Locate and identify every blood parasite.
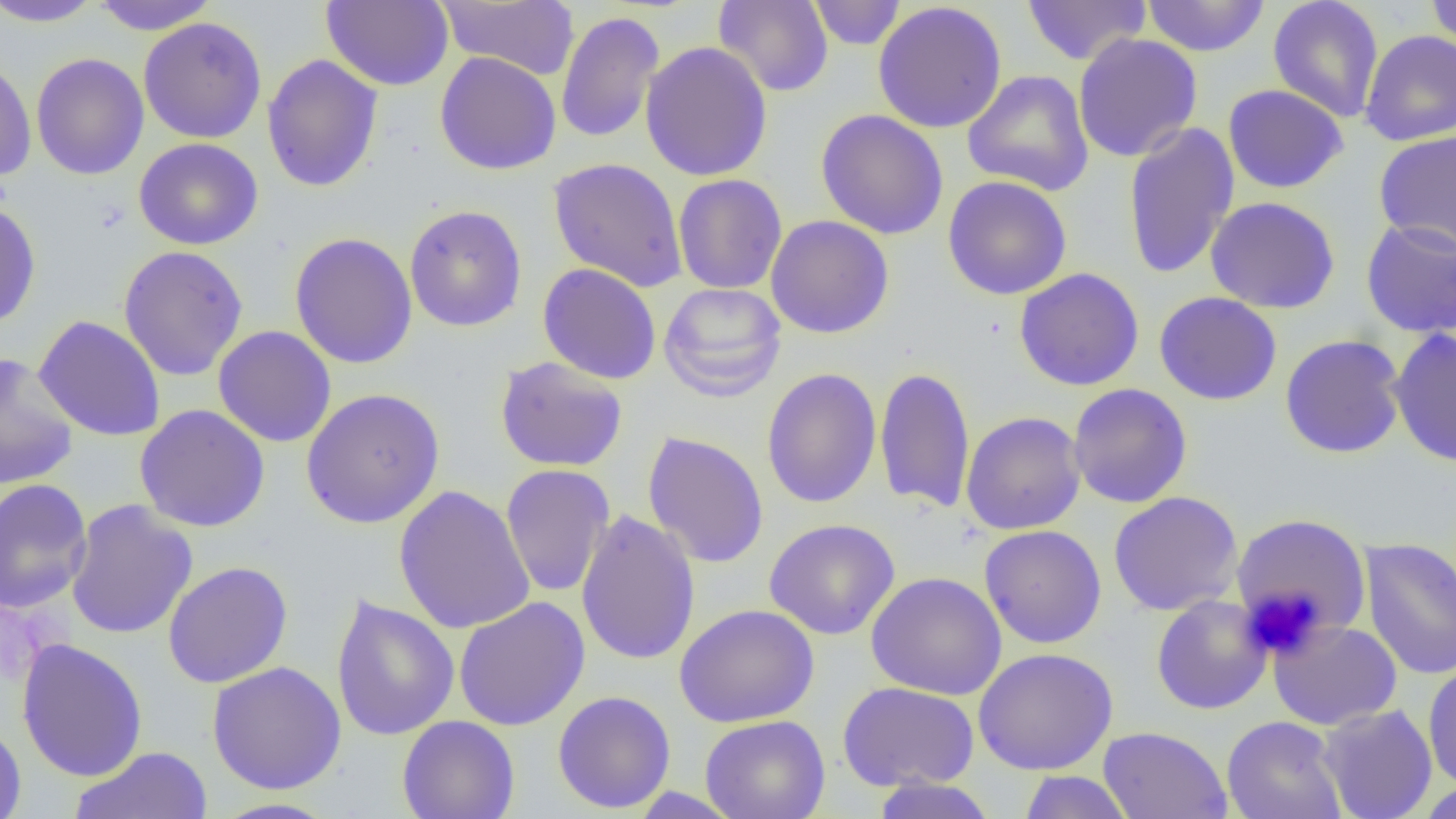

No blood parasites seen.

Approximate bounding boxes as (x1,y1)-(x2,y2) corner pairs in pixels. Platelet locations: (1242,587)-(1326,659). Uninfected red blood cell locations: (0,0)-(105,28), (89,0)-(220,35), (322,0)-(453,90), (437,0)-(579,80), (713,0)-(834,97), (807,0)-(906,50), (1021,0)-(1152,66), (1141,0)-(1270,57), (1425,0)-(1456,53), (1268,1)-(1384,123), (872,2)-(1008,134), (555,10)-(665,144), (138,17)-(267,144), (1360,29)-(1456,146), (1072,33)-(1203,162), (640,41)-(773,182), (434,52)-(562,175), (30,53)-(149,180), (0,54)-(37,182), (262,54)-(383,193), (962,70)-(1094,196), (1223,84)-(1349,193), (815,109)-(949,240), (1122,121)-(1239,281), (1373,130)-(1456,254), (134,137)-(264,251), (547,157)-(688,292), (673,174)-(787,294), (943,175)-(1072,300), (1204,196)-(1341,314), (0,199)-(41,330), (404,204)-(527,332), (766,214)-(894,339), (1361,218)-(1456,338), (289,232)-(417,370), (118,245)-(249,380), (537,263)-(662,384), (1014,267)-(1145,391), (658,282)-(787,402), (1154,291)-(1282,405), (34,315)-(166,441), (213,326)-(337,448), (1388,326)-(1456,467), (1279,334)-(1407,458), (0,352)-(79,490), (495,356)-(629,473), (875,365)-(975,514), (761,368)-(882,509), (1067,383)-(1192,508), (301,387)-(445,528), (135,404)-(271,532), (960,411)-(1086,535), (642,431)-(769,569), (500,463)-(614,598), (0,478)-(93,613), (393,485)-(535,635), (1108,491)-(1243,615), (65,500)-(197,640), (576,509)-(701,666), (1232,512)-(1373,640), (764,518)-(900,640), (979,525)-(1107,649), (1359,537)-(1456,680), (163,561)-(293,688), (866,572)-(1006,700), (331,595)-(460,741), (1151,595)-(1272,715), (453,596)-(590,731), (674,603)-(819,727), (1268,619)-(1402,730), (16,638)-(148,782), (973,647)-(1118,775), (207,661)-(347,794), (1423,661)-(1456,792), (837,681)-(979,792), (552,691)-(677,813), (1316,704)-(1438,819), (700,714)-(831,819), (397,715)-(520,819), (1222,715)-(1347,819), (0,721)-(26,819), (1097,726)-(1233,819), (69,746)-(212,819), (1017,771)-(1135,818), (870,778)-(999,819), (1413,780)-(1456,819), (628,787)-(744,818), (211,797)-(342,818). Slide-level diagnosis: no evidence of blood parasites. Thin blood film. One field of a larger specimen. Captured at 1000x magnification. Image is 1456×819 pixels. Light microscopy.